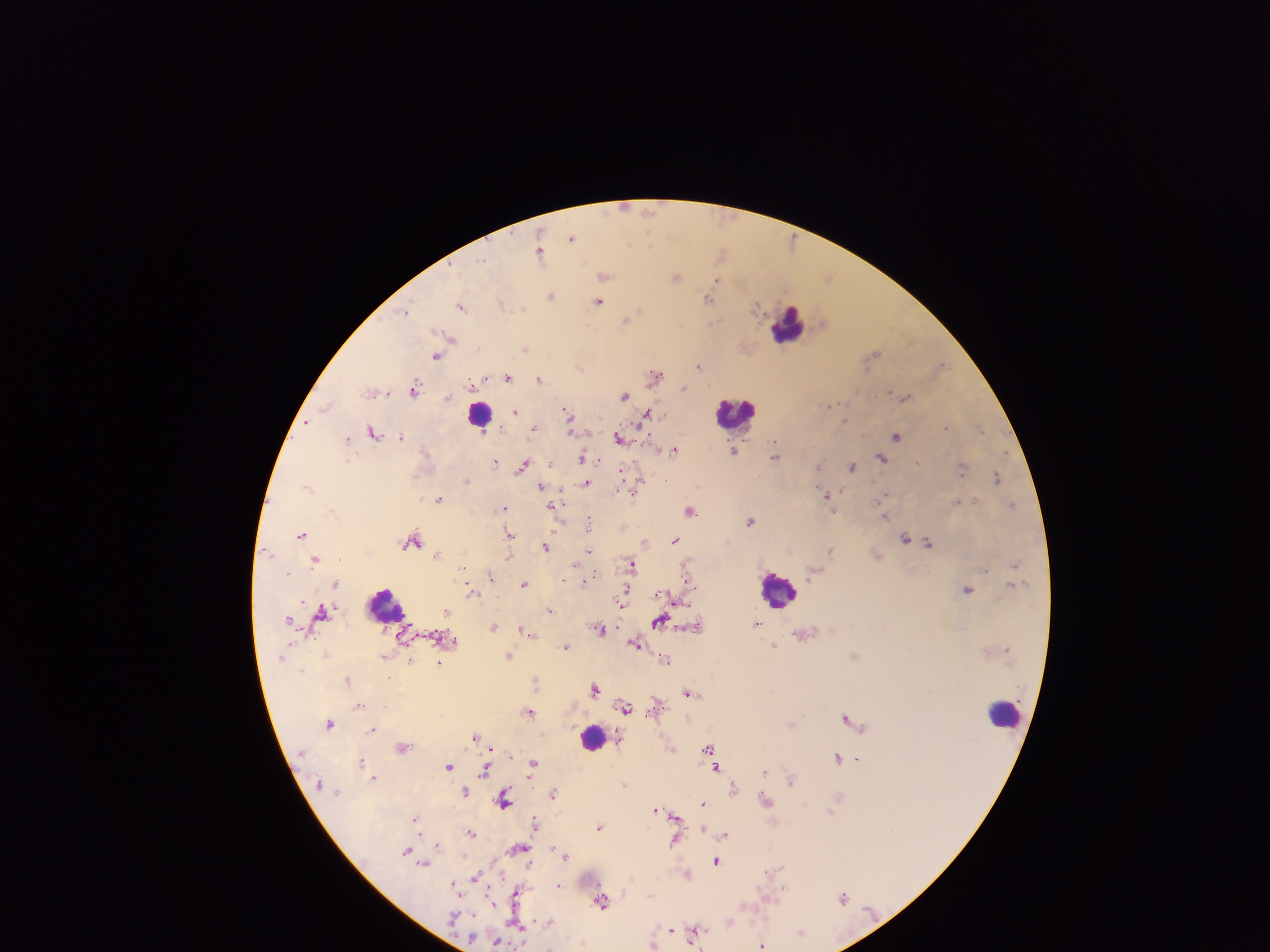

Approximate centers as [x, y] in pixels.
Summary:
  - Leukocyte locations: [789, 324], [735, 412], [480, 413], [779, 589], [385, 609], [1004, 713], [593, 738]
  - Malaria parasite locations: [625, 207], [649, 211], [572, 237], [539, 252], [722, 252], [483, 260], [604, 275], [675, 277], [829, 277], [716, 280], [550, 296], [709, 299], [598, 302], [501, 303], [461, 305], [757, 306], [407, 309], [640, 312], [627, 319], [453, 339], [525, 348], [873, 353], [437, 356], [940, 365], [698, 366], [580, 367], [656, 374], [508, 378], [539, 378], [471, 383], [683, 388], [414, 389], [372, 391], [890, 391], [388, 394], [625, 395], [447, 397], [906, 397], [832, 405], [326, 406], [516, 411], [568, 412], [645, 416], [307, 423], [570, 427], [946, 427], [533, 428], [501, 429], [981, 430], [374, 432], [897, 436], [402, 437], [620, 438], [348, 439], [775, 443], [675, 450], [734, 450], [775, 456], [582, 457], [881, 458], [495, 460], [523, 465], [853, 465], [819, 466], [962, 469], [997, 477], [466, 480], [665, 480], [587, 483], [309, 486], [541, 486], [638, 486], [635, 492], [828, 495], [886, 495], [439, 499], [957, 502], [1013, 504], [553, 507], [505, 508], [690, 510], [833, 512], [884, 516], [750, 521], [589, 527], [301, 534], [509, 535], [905, 537], [675, 540], [413, 541], [928, 542], [645, 543], [545, 547], [589, 550], [268, 551], [831, 551], [438, 554], [509, 557], [316, 560], [633, 564], [1015, 564], [575, 565], [463, 568], [986, 569], [288, 573], [492, 576], [688, 582], [524, 583], [335, 584], [583, 584], [967, 589], [472, 591], [663, 594], [622, 601], [550, 610], [321, 611], [288, 618], [659, 622], [757, 623], [494, 627], [601, 629], [524, 631], [454, 640], [635, 643], [775, 646], [566, 647], [509, 656], [665, 659], [410, 660], [439, 663], [347, 680], [596, 689], [690, 693], [657, 703], [359, 705], [625, 707], [529, 712], [846, 717], [329, 723], [793, 723], [373, 730], [475, 735], [403, 747], [709, 748], [673, 749], [838, 757], [858, 758], [361, 761], [533, 764], [449, 766], [716, 767], [484, 771], [764, 772], [373, 776], [792, 780], [624, 783], [734, 788], [464, 792], [554, 794], [838, 798], [766, 800], [504, 801], [704, 803], [656, 809], [673, 815], [414, 820], [535, 823], [600, 827], [703, 829], [471, 833], [725, 835], [675, 841], [437, 844], [519, 849], [407, 851], [564, 854], [716, 861], [423, 863], [688, 873], [476, 877], [558, 884], [454, 885], [784, 889], [515, 896], [843, 897], [602, 902], [729, 921], [547, 922], [671, 929], [696, 931], [801, 932], [496, 941], [763, 944]
  - Image size: 1270×952 pixels
  - Preparation: thick blood smear
  - Country: Ghana
  - Capture: mobile-phone photograph through a microscope
  - Field of view: single